Identify the blood parasite species.
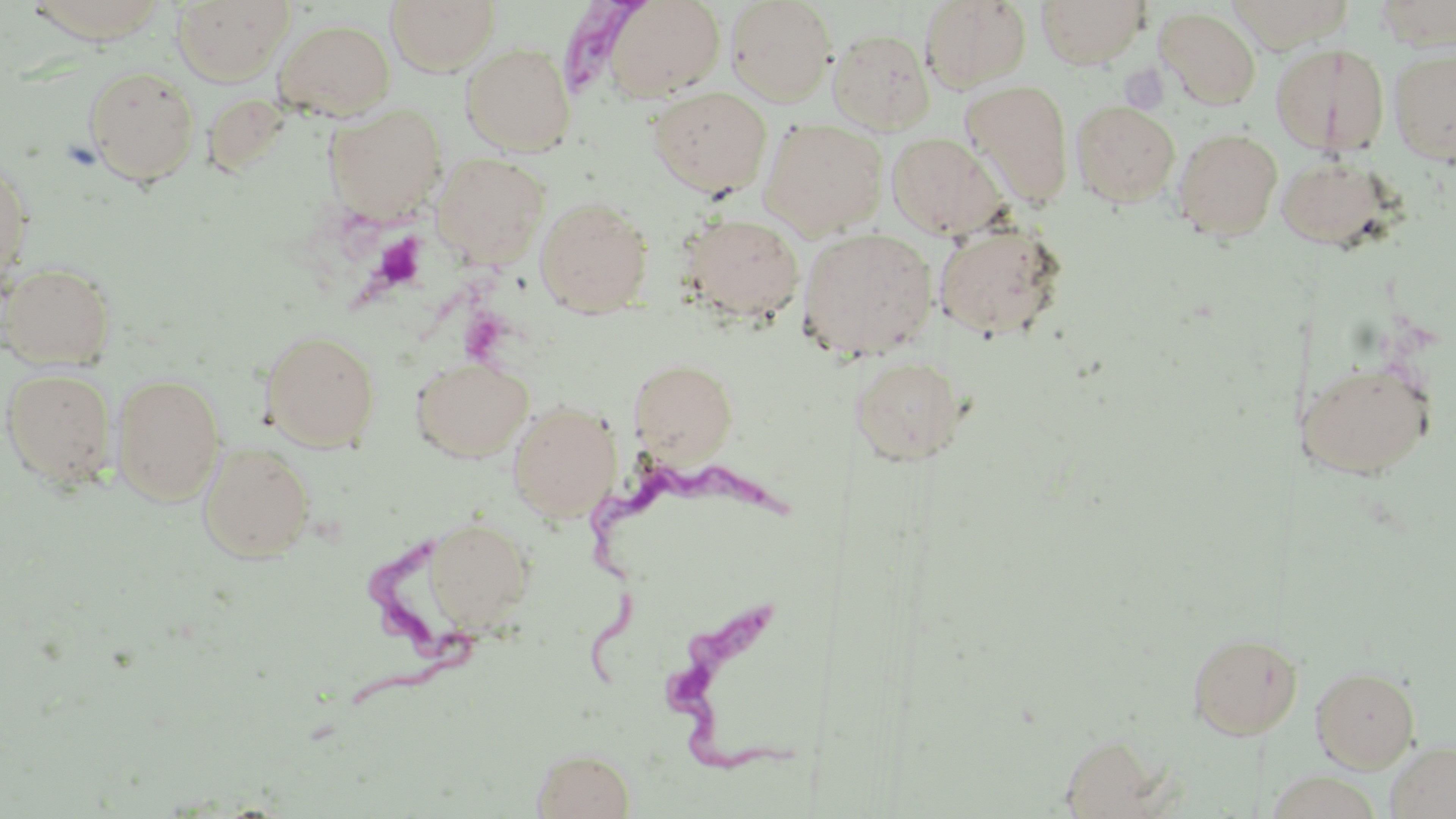
Trypanosoma brucei.

Summary:
  - Coordinate format: approximate bounding boxes as [x1, y1, x2, y2] in pixels
  - Uninfected red blood cell locations: [172, 0, 294, 84], [385, 0, 500, 75], [603, 0, 725, 102], [724, 0, 837, 106], [1035, 0, 1149, 68], [20, 1, 176, 44], [920, 1, 1032, 91], [1156, 7, 1261, 108], [274, 18, 395, 120], [828, 28, 936, 135], [1270, 42, 1390, 158], [461, 43, 576, 156], [1388, 47, 1456, 166], [83, 65, 200, 184], [961, 80, 1074, 206], [649, 87, 772, 197], [1071, 100, 1179, 206], [324, 104, 447, 220], [760, 118, 888, 238], [1172, 127, 1283, 240], [887, 131, 1007, 239], [431, 152, 549, 267], [0, 153, 34, 292], [1275, 154, 1394, 249], [535, 196, 653, 318], [679, 213, 804, 324], [933, 222, 1067, 341], [797, 227, 938, 361], [1, 260, 117, 369], [260, 329, 381, 451], [412, 356, 534, 461], [851, 356, 965, 466], [629, 359, 738, 463], [1301, 360, 1435, 478], [2, 367, 118, 487], [111, 373, 225, 505], [508, 400, 621, 523], [199, 441, 315, 562], [424, 517, 534, 633], [1187, 631, 1272, 739], [1268, 637, 1300, 740], [1311, 665, 1421, 772], [1386, 741, 1456, 819], [532, 748, 636, 819]
  - Platelet locations: [374, 234, 427, 289]
  - Trypanosoma brucei locations: [544, 2, 647, 96], [582, 458, 791, 692], [343, 542, 483, 713], [669, 609, 819, 782]
  - Field of view: single
  - Stain: May-Grünwald-Giemsa
  - Preparation: thin blood film
  - Magnification: 1000x
  - Modality: optical microscopy
  - Image size: 1456×819 pixels